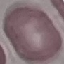 Malaria status: uninfected. Acquired by smartphone through the microscope eyepiece. Automatically extracted cell patch, resized to 64 × 64 pixels. Giemsa-stained preparation. Thin blood smear.